Assess for Plasmodium parasites.
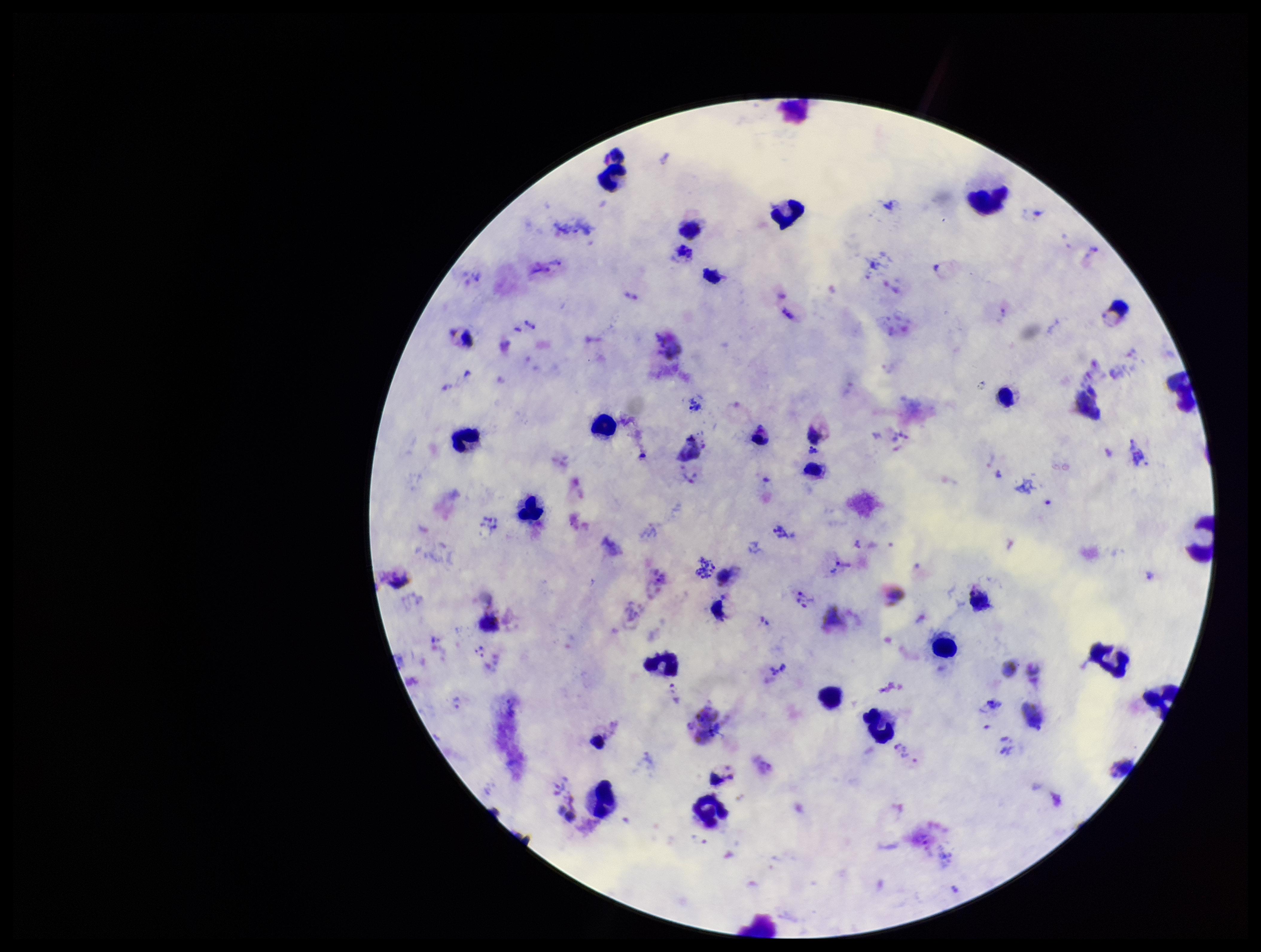
Identified.

field of view = one from this slide
parasite count = 26
image size = 1261×952 pixels
species reported for this patient = Plasmodium vivax
patient malaria status = positive
stain = Giemsa
capture = smartphone photograph through the microscope eyepiece
preparation = thick blood smear
leukocyte count = 21